Classify this cell by malaria status.
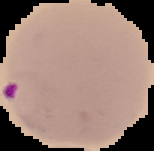

Parasitized.

Image is 154×151 pixels. From a thin blood smear. Segmented cell region on a black background.